Give the extent of all uninfected red blood cells.
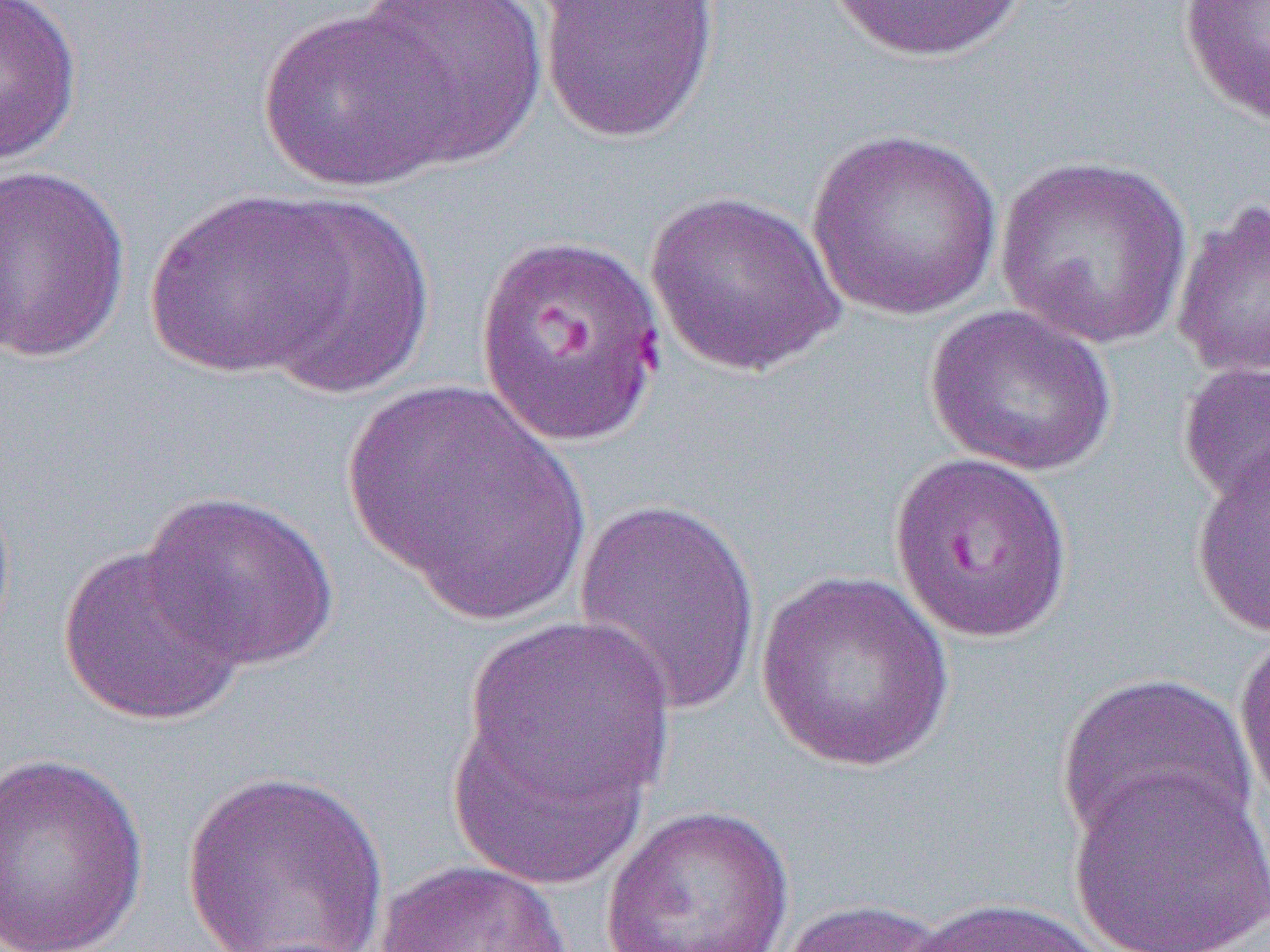

Approximate bounding boxes as (x1, y1, x2, y2) in pixels.
Uninfected red blood cells: (0, 0, 84, 166), (351, 0, 549, 170), (827, 0, 1029, 64), (1177, 0, 1270, 126), (537, 1, 721, 144), (257, 8, 457, 192), (806, 127, 1005, 322), (994, 153, 1195, 350), (0, 163, 133, 363), (143, 189, 352, 379), (644, 189, 846, 377), (1171, 196, 1270, 380), (252, 197, 436, 400), (470, 230, 669, 449), (924, 304, 1119, 478), (1177, 360, 1270, 511), (341, 378, 591, 623), (1190, 443, 1270, 636), (888, 452, 1075, 643), (140, 490, 341, 672), (571, 496, 766, 721), (57, 541, 249, 728), (753, 570, 956, 772), (458, 617, 678, 828), (1234, 624, 1270, 808), (1056, 671, 1259, 854), (445, 694, 657, 896), (0, 751, 151, 951), (1067, 765, 1270, 952), (181, 768, 390, 951), (601, 804, 796, 952), (375, 859, 577, 952), (898, 895, 1122, 952), (775, 897, 959, 952).

Slide-level diagnosis: Plasmodium falciparum. Thin blood film. 1000x magnification. Single field of view. Light microscopy. Image is 1270×952 pixels.